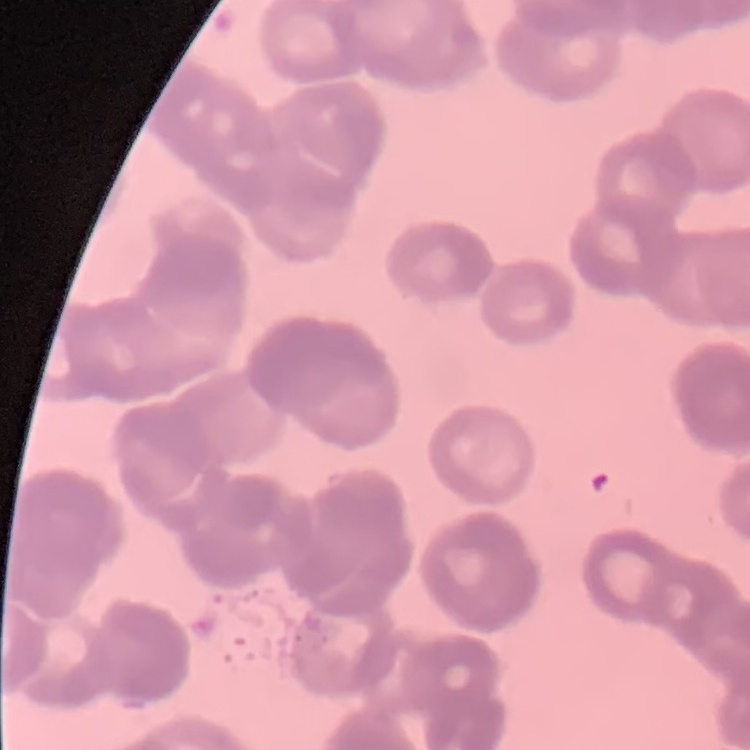
The red blood cells exhibit rouleaux formation. Stained with either Field's or Giemsa. One tile cut from a larger photomicrograph. Thin peripheral smear.